Locate and identify every blood parasite.
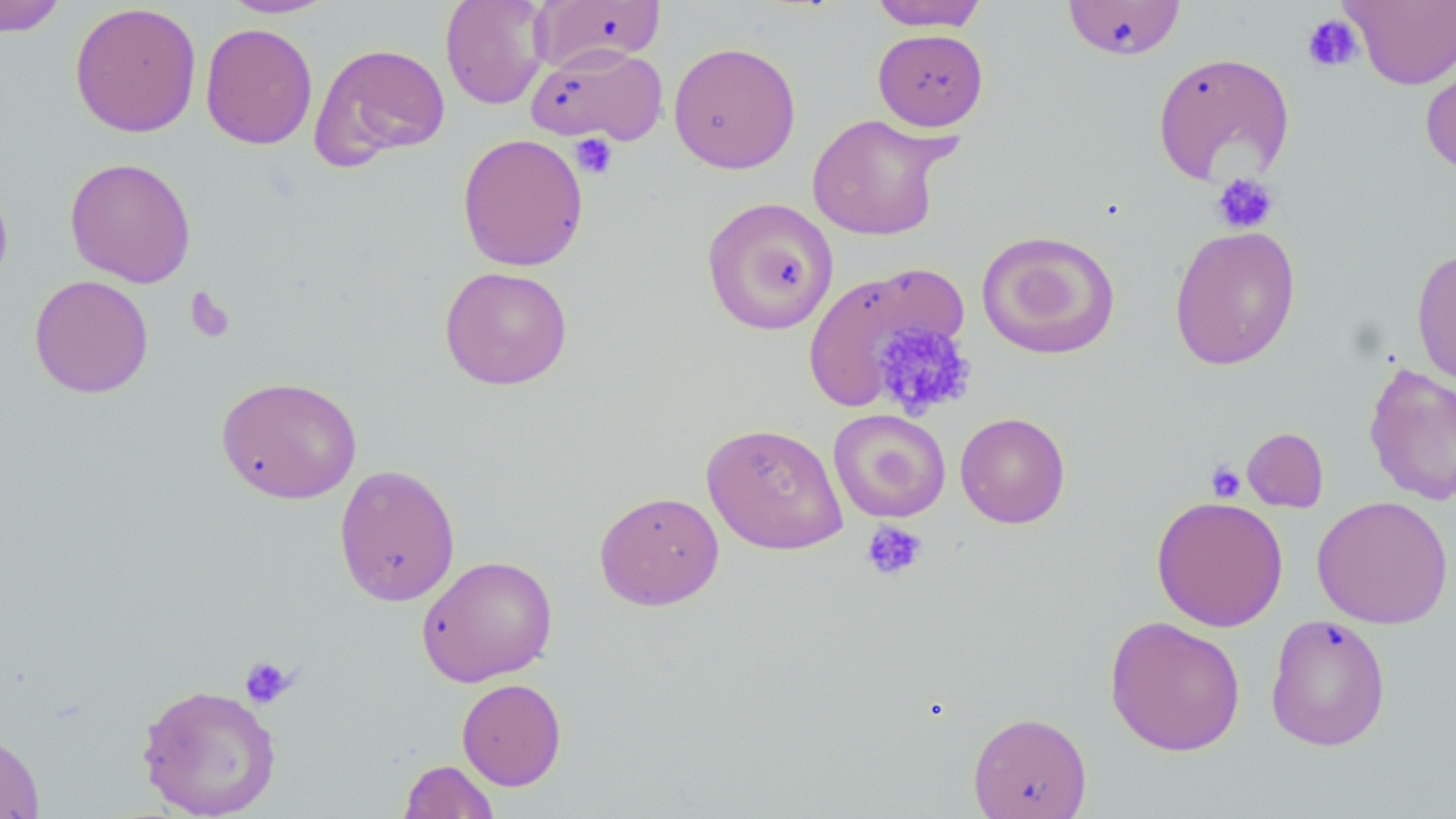
No blood parasites observed.

Approximate bounding boxes as (x1, y1, x2, y2) in pixels. Uninfected red blood cell locations: (0, 0, 68, 36), (221, 0, 336, 18), (440, 0, 552, 110), (1062, 0, 1186, 60), (1342, 0, 1456, 90), (531, 1, 666, 73), (869, 1, 989, 31), (69, 2, 202, 138), (200, 23, 318, 150), (873, 29, 989, 131), (668, 41, 801, 174), (309, 42, 451, 168), (525, 44, 668, 147), (1152, 51, 1295, 187), (1420, 51, 1456, 179), (806, 112, 953, 241), (457, 132, 589, 272), (64, 156, 197, 288), (0, 176, 13, 298), (701, 196, 839, 336), (1168, 224, 1301, 370), (975, 229, 1122, 361), (1411, 248, 1456, 386), (802, 261, 968, 414), (439, 265, 574, 391), (28, 274, 154, 398), (1363, 362, 1456, 507), (216, 375, 362, 504), (828, 409, 951, 524), (955, 412, 1071, 528), (701, 422, 848, 555), (1242, 427, 1329, 512), (333, 464, 460, 606), (594, 490, 724, 611), (1150, 495, 1289, 632), (1311, 495, 1453, 629), (416, 554, 558, 687), (1265, 614, 1391, 751), (1104, 615, 1246, 756), (456, 678, 567, 790), (136, 682, 281, 818), (967, 711, 1092, 819), (0, 732, 45, 819), (398, 759, 500, 819). Platelet locations: (1301, 13, 1364, 73), (569, 133, 618, 179), (1211, 173, 1279, 234), (185, 287, 237, 345), (872, 321, 976, 420), (1206, 460, 1247, 503), (862, 520, 927, 581), (238, 655, 297, 709). Slide-level diagnosis: no evidence of blood parasites. 1000x magnification. May-Grünwald-Giemsa stain. Thin blood film. Optical microscopy. Image is 1456×819 pixels. Single field of view.